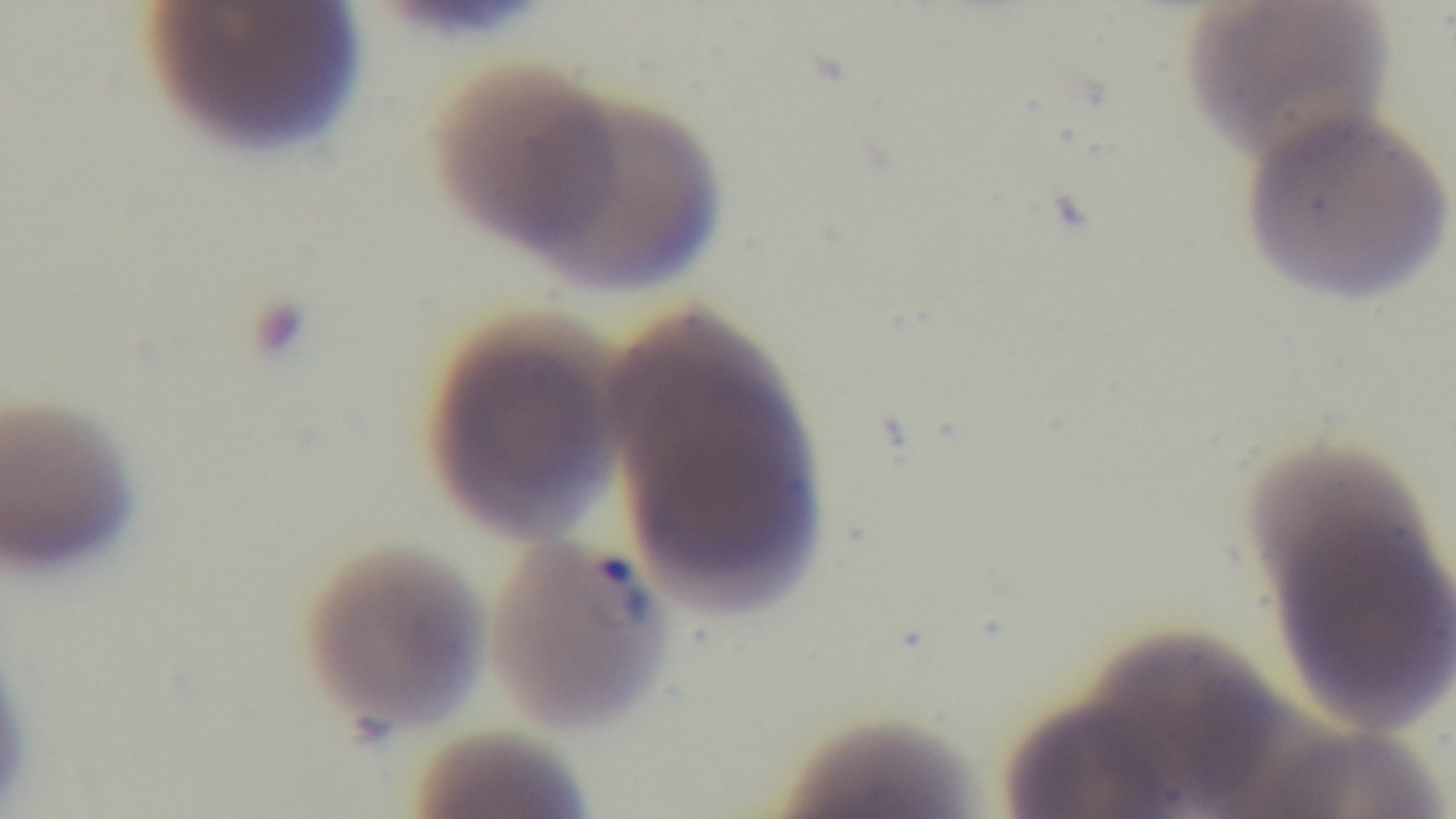
modality = light microscopy
field of view = one from the slide
malaria status = positive
capture = mounted 4K digital camera
stain = Giemsa
objective = 100x oil immersion
preparation = thin smear